Assess the background quality.
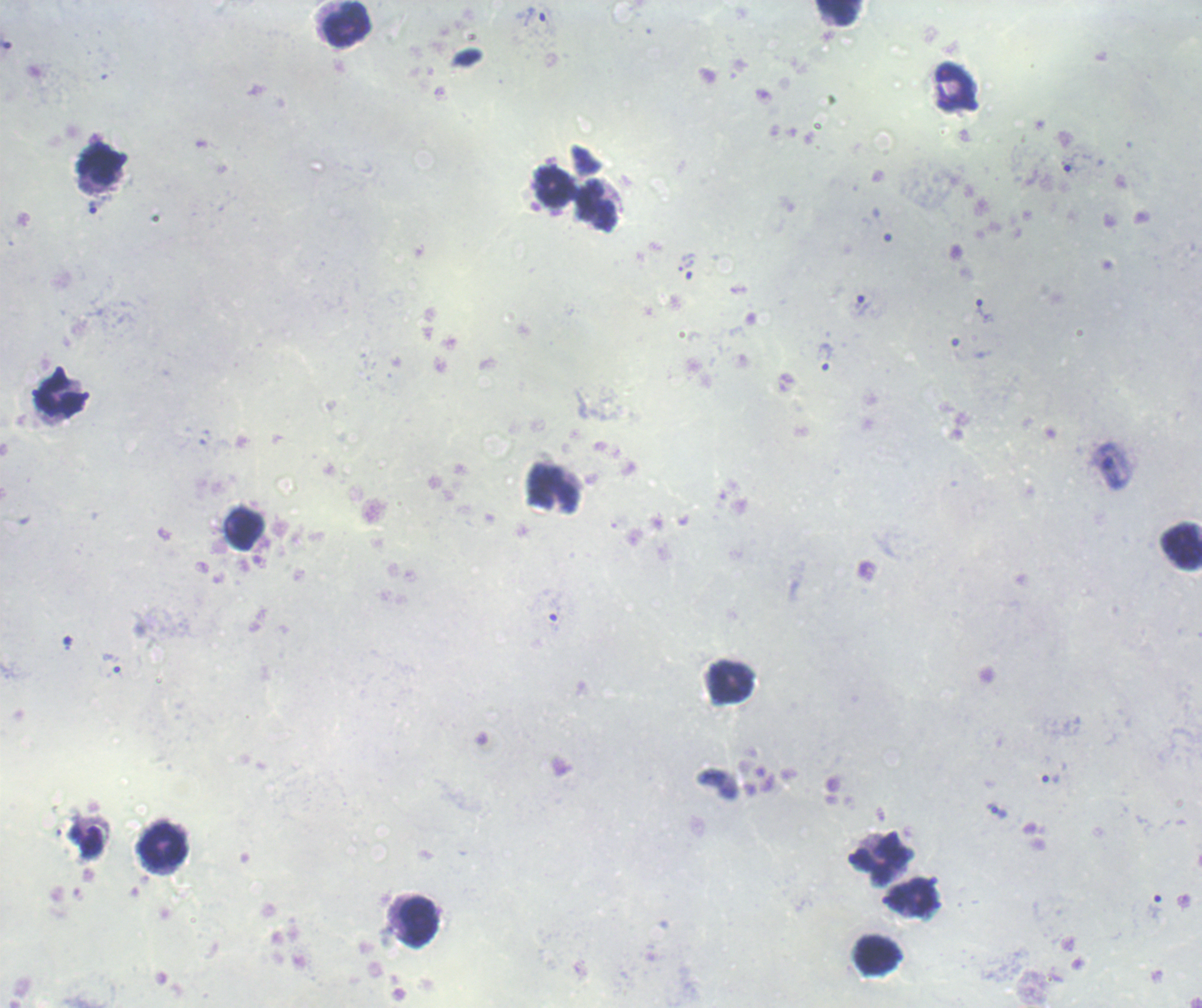

Unsatisfactory.

Approximate centers as [x, y] in pixels. Trophozoite locations: [531, 17], [98, 204], [862, 304], [981, 311], [824, 355], [1051, 779]. Leukocyte locations: [838, 12], [347, 23], [954, 86], [97, 165], [553, 187], [597, 205], [61, 397], [553, 488], [244, 529], [1182, 545], [730, 683], [163, 845], [881, 859], [912, 897], [418, 922], [876, 954]. Image is 1202×1008 pixels. 100x magnification. Previously used in a real diagnosis. Result: malaria parasites identified. One field from this slide. Romanowsky stain. Thick blood smear.